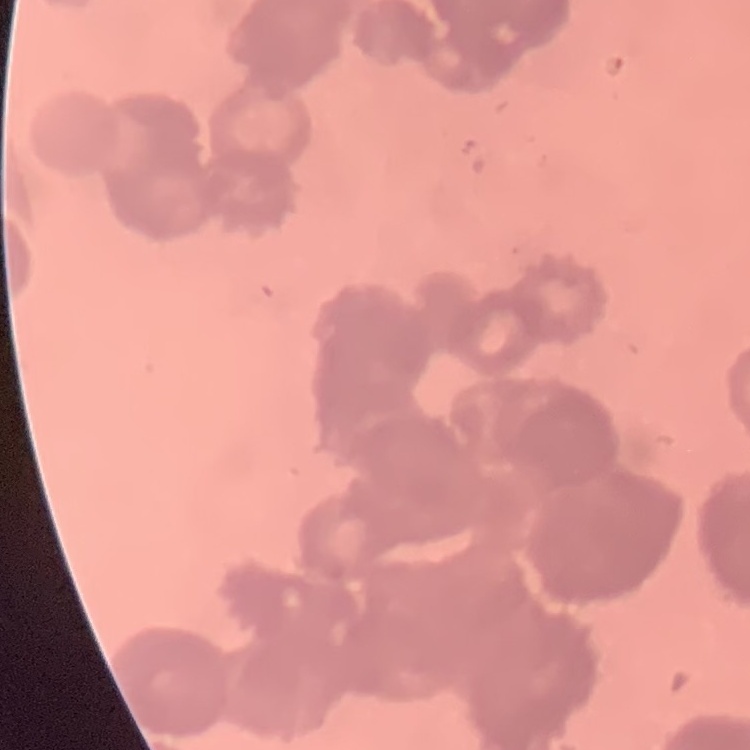 The erythrocytes exhibit rouleaux formation. One tile cut from a larger photomicrograph. Field's or Giemsa stain. Thin blood smear.